Report the malaria status of this cell.
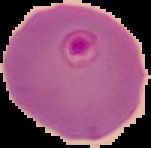
Parasitized.

Summary:
  - Preparation: thin blood film
  - Image size: 151×148 pixels
  - Image type: segmented cell region on a black background